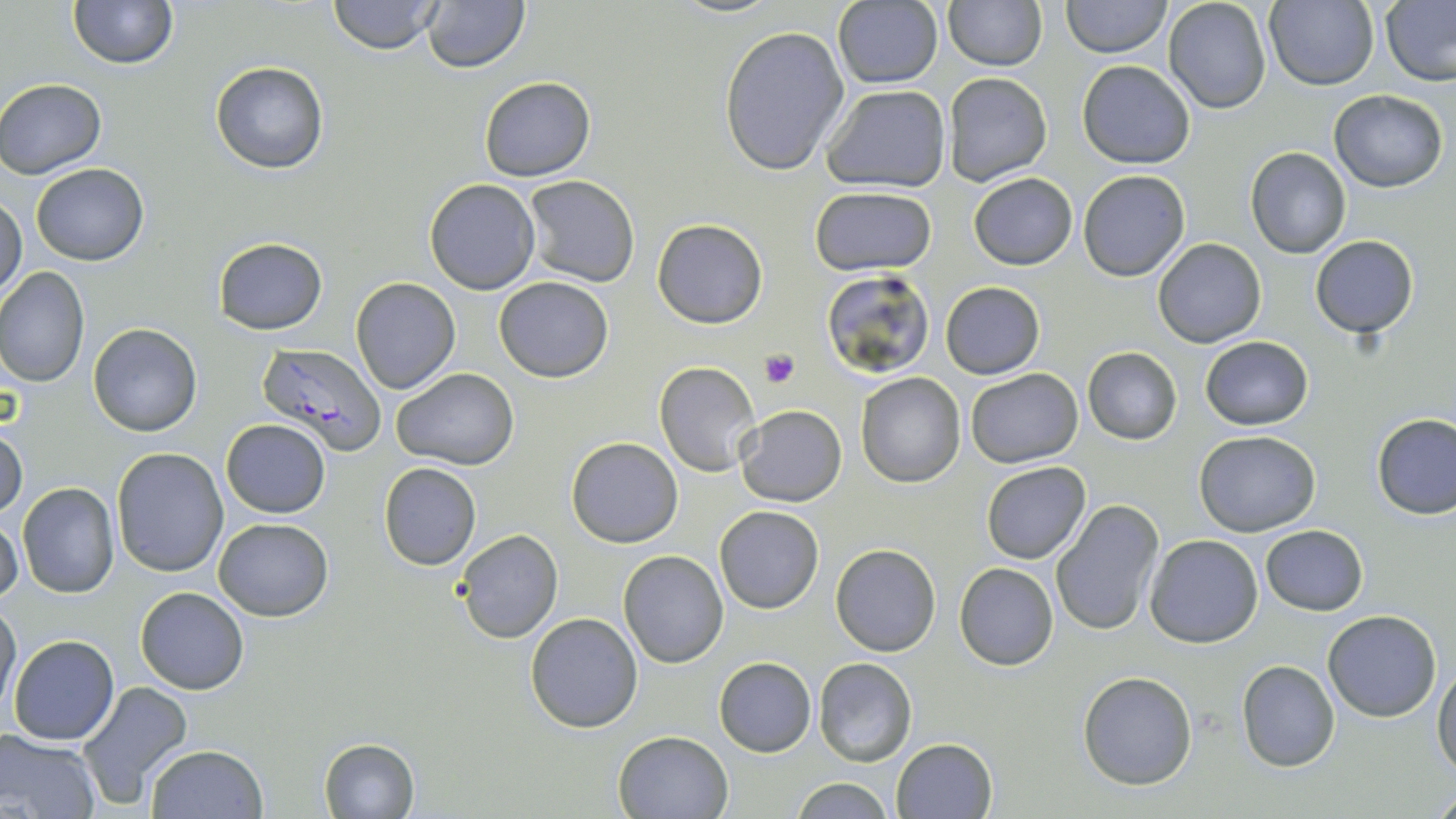

Summary:
  - Coordinate format: approximate bounding boxes as (x1, y1, x2, y2) in pixels
  - Platelet locations: (759, 349, 800, 387)
  - Plasmodium falciparum-infected red blood cell locations: (259, 345, 386, 455)
  - Uninfected red blood cell locations: (68, 0, 177, 69), (327, 0, 443, 54), (421, 0, 530, 73), (666, 0, 782, 18), (1061, 0, 1170, 58), (1162, 0, 1272, 114), (1265, 0, 1379, 91), (1380, 0, 1456, 88), (831, 1, 943, 87), (943, 2, 1045, 71), (718, 26, 850, 175), (1078, 60, 1196, 168), (210, 62, 328, 173), (942, 72, 1052, 186), (479, 75, 595, 181), (0, 78, 107, 179), (820, 85, 952, 194), (1331, 91, 1447, 191), (1245, 147, 1352, 259), (30, 164, 150, 265), (1078, 170, 1190, 281), (969, 173, 1077, 270), (522, 176, 641, 288), (424, 179, 540, 294), (808, 186, 938, 276), (0, 193, 27, 301), (652, 218, 768, 329), (1310, 236, 1419, 337), (213, 237, 327, 334), (1154, 238, 1265, 348), (0, 266, 91, 388), (821, 269, 935, 379), (494, 276, 613, 382), (350, 277, 461, 395), (940, 282, 1045, 378), (88, 323, 202, 436), (1199, 336, 1314, 430), (1083, 347, 1182, 444), (654, 362, 761, 476), (965, 367, 1084, 469), (392, 368, 519, 469), (855, 372, 966, 488), (735, 403, 847, 506), (1372, 414, 1456, 520), (221, 419, 331, 518), (0, 426, 27, 519), (1193, 429, 1321, 536), (566, 437, 683, 549), (111, 447, 228, 577), (980, 462, 1092, 563), (378, 463, 482, 569), (18, 482, 120, 598), (1052, 500, 1164, 636), (714, 505, 824, 614), (0, 515, 24, 606), (213, 517, 334, 620), (1260, 524, 1368, 615), (452, 529, 564, 644), (1144, 534, 1263, 648), (830, 543, 940, 656), (618, 549, 729, 669), (954, 563, 1058, 670), (136, 586, 248, 694), (0, 598, 21, 712), (1322, 610, 1443, 721), (525, 611, 643, 732), (8, 635, 119, 746), (714, 656, 817, 757), (813, 657, 917, 766), (1238, 660, 1340, 772), (1433, 661, 1456, 778), (1078, 671, 1197, 789), (77, 681, 193, 806), (613, 729, 732, 818), (0, 730, 102, 817), (317, 737, 421, 819), (891, 738, 997, 819), (146, 744, 268, 819), (787, 777, 900, 818), (1431, 783, 1456, 815)
  - Slide-level diagnosis: Plasmodium falciparum
  - Stain: May-Grünwald-Giemsa
  - Magnification: 1000x
  - Field of view: single
  - Preparation: thin blood smear
  - Image size: 1456×819 pixels
  - Modality: light microscopy